Name the cell type shown.
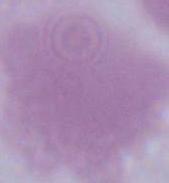
This is an erythrocyte.

Summary:
  - Modality: photomicrograph
  - Magnification: 1000x